Report the malaria status of this cell.
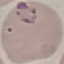
Parasitized.

capture = smartphone camera at the microscope eyepiece
image type = cell patch, automatically extracted from a larger field of view and resized to 64 × 64 pixels
preparation = thin smear
stain = Giemsa